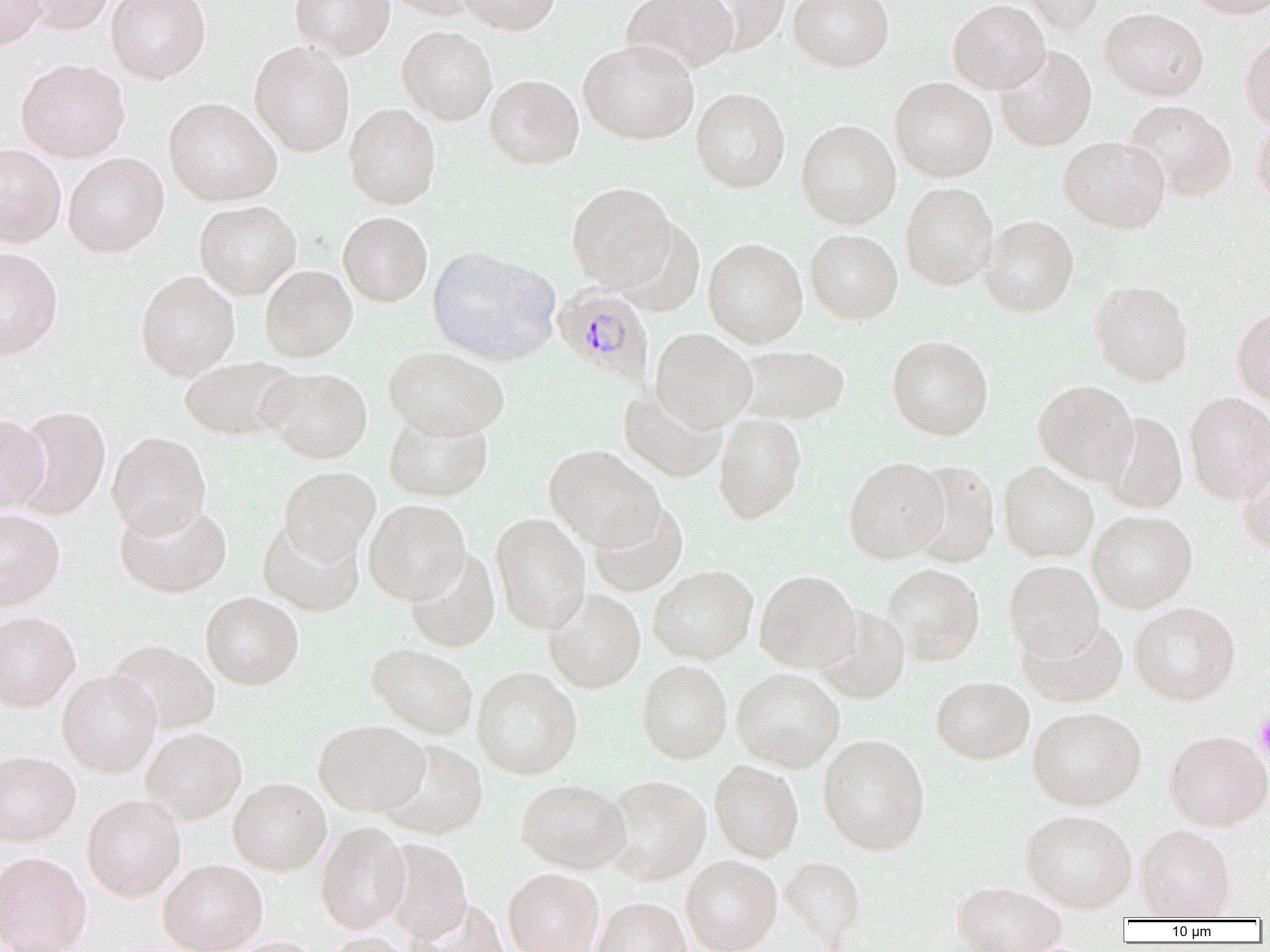

Summary:
  - Coordinate format: approximate bounding boxes as [x1, y1, x2, y2] in pixels
  - Plasmodium malariae-infected red blood cell locations: [553, 284, 654, 388]
  - Platelet locations: [1254, 711, 1270, 760]
  - Uninfected red blood cell locations: [0, 0, 47, 50], [17, 0, 115, 34], [106, 0, 211, 84], [290, 0, 394, 61], [384, 0, 485, 20], [458, 0, 560, 35], [622, 0, 739, 76], [690, 0, 792, 56], [788, 0, 894, 72], [948, 0, 1050, 94], [1020, 0, 1106, 35], [1186, 0, 1269, 18], [1101, 7, 1208, 101], [397, 25, 497, 125], [1240, 33, 1270, 131], [579, 39, 699, 145], [249, 42, 355, 157], [995, 46, 1097, 152], [16, 58, 130, 162], [485, 74, 583, 169], [890, 77, 997, 182], [691, 88, 790, 193], [164, 97, 282, 206], [1123, 100, 1236, 202], [344, 104, 441, 209], [1251, 116, 1270, 210], [796, 119, 901, 229], [1058, 135, 1170, 234], [0, 144, 66, 246], [63, 152, 168, 257], [566, 182, 676, 292], [900, 182, 998, 291], [194, 200, 301, 299], [338, 211, 433, 307], [978, 215, 1078, 318], [612, 219, 705, 318], [804, 228, 903, 325], [703, 238, 808, 347], [428, 246, 560, 366], [0, 247, 63, 359], [260, 265, 357, 362], [135, 270, 240, 381], [1090, 280, 1193, 386], [1232, 305, 1270, 406], [649, 328, 757, 432], [887, 335, 994, 440], [735, 344, 851, 425], [383, 346, 510, 440], [178, 356, 300, 441], [259, 367, 373, 463], [1033, 380, 1138, 484], [618, 387, 727, 483], [1184, 392, 1270, 503], [11, 406, 111, 520], [713, 412, 807, 524], [1098, 412, 1187, 514], [0, 413, 50, 512], [383, 413, 493, 502], [107, 431, 211, 538], [544, 444, 664, 550], [1237, 449, 1270, 557], [844, 456, 948, 563], [907, 460, 1000, 568], [998, 461, 1099, 562], [278, 466, 381, 563], [114, 499, 232, 599], [363, 499, 470, 605], [589, 501, 688, 597], [0, 509, 65, 611], [1087, 509, 1197, 613], [491, 512, 591, 634], [257, 519, 364, 617], [404, 549, 500, 652], [1004, 560, 1104, 659], [880, 563, 985, 665], [648, 565, 758, 664], [755, 569, 860, 673], [543, 588, 645, 693], [200, 592, 304, 690], [1129, 600, 1241, 704], [813, 605, 910, 704], [0, 611, 80, 711], [1018, 616, 1128, 708], [106, 639, 220, 735], [367, 643, 479, 739], [637, 660, 732, 764], [472, 666, 582, 779], [732, 667, 845, 772], [57, 669, 162, 777], [931, 675, 1034, 764], [1028, 706, 1146, 810], [314, 720, 429, 816], [141, 727, 247, 824], [1164, 729, 1270, 831], [817, 733, 930, 855], [378, 738, 488, 840], [0, 750, 81, 847], [709, 760, 804, 862], [603, 774, 711, 885], [228, 777, 331, 875], [515, 777, 630, 873], [82, 794, 186, 901], [1020, 809, 1137, 912], [315, 821, 411, 933], [1135, 823, 1237, 920], [379, 838, 473, 941], [0, 851, 91, 952], [681, 854, 782, 952], [780, 856, 867, 946], [159, 858, 267, 952], [503, 868, 603, 952], [951, 883, 1068, 950], [592, 897, 691, 952], [409, 899, 510, 952], [319, 933, 416, 952], [221, 937, 323, 952]
  - Slide-level diagnosis: Plasmodium malariae
  - Image size: 1270×952 pixels
  - Magnification: 1000x
  - Modality: light microscopy
  - Preparation: thin blood film
  - Field of view: single